Locate and identify every blood parasite.
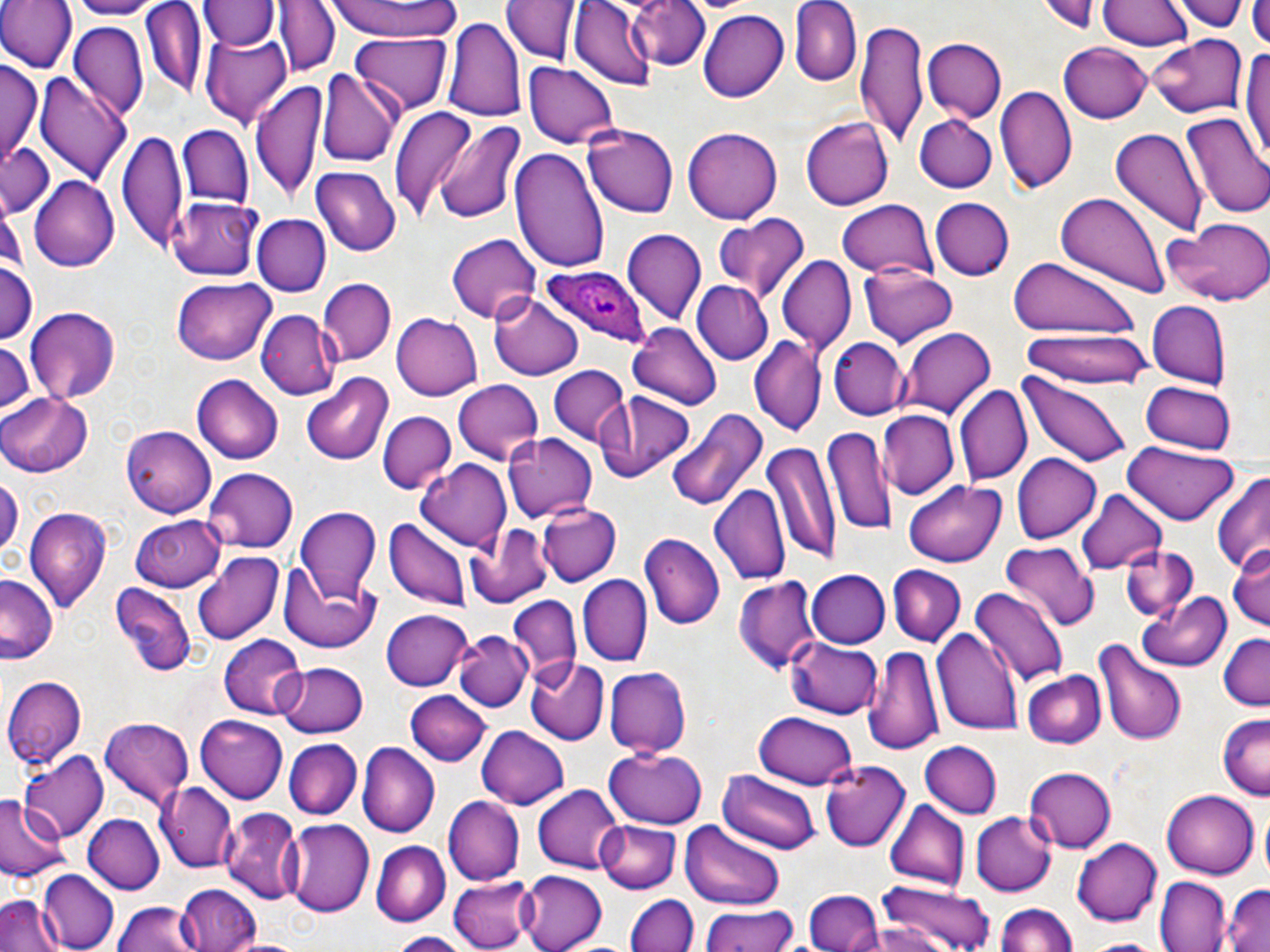
Approximate bounding boxes as (x1,y1)-(x2,y2) corner pairs in pixels.
Plasmodium ovale-infected red blood cells: (543,264)-(653,347).
No Plasmodium falciparum, Plasmodium malariae, Plasmodium vivax, Babesia divergens, or Trypanosoma brucei observed.

Uninfected red blood cell locations: (0,0)-(76,73), (65,0)-(161,18), (202,0)-(274,50), (275,0)-(338,77), (328,0)-(464,42), (787,0)-(860,87), (1039,0)-(1103,34), (1098,0)-(1191,52), (1174,0)-(1249,31), (1249,0)-(1270,48), (503,1)-(578,65), (569,1)-(655,88), (630,1)-(711,72), (139,2)-(207,99), (697,9)-(788,102), (443,17)-(526,125), (856,22)-(926,149), (69,23)-(147,122), (201,26)-(292,125), (353,33)-(451,113), (1146,33)-(1245,117), (920,37)-(1003,121), (1060,42)-(1152,124), (1240,48)-(1269,163), (2,60)-(41,159), (523,62)-(617,149), (319,68)-(400,170), (36,74)-(131,184), (251,78)-(322,209), (998,85)-(1077,194), (389,103)-(475,221), (1180,109)-(1270,221), (915,113)-(999,192), (430,117)-(528,228), (802,117)-(893,210), (177,124)-(253,207), (582,124)-(678,219), (118,127)-(186,252), (682,127)-(783,226), (1110,129)-(1208,235), (2,140)-(56,214), (510,147)-(610,271), (315,165)-(403,256), (29,177)-(119,271), (1054,192)-(1171,298), (166,196)-(263,281), (930,198)-(1014,281), (835,199)-(939,280), (713,213)-(812,302), (251,214)-(330,296), (1165,217)-(1270,306), (622,231)-(706,326), (447,234)-(542,324), (776,254)-(856,352), (1008,255)-(1142,351), (0,256)-(38,345), (859,266)-(958,347), (172,278)-(277,366), (319,280)-(395,364), (694,281)-(772,363), (489,292)-(584,381), (1146,300)-(1231,387), (25,306)-(121,403), (257,309)-(338,399), (391,312)-(483,402), (628,321)-(722,408), (895,326)-(995,422), (1022,331)-(1152,388), (0,336)-(36,420), (748,336)-(825,437), (829,337)-(906,419), (548,366)-(630,448), (302,373)-(394,464), (1014,373)-(1132,470), (194,374)-(282,464), (453,379)-(545,466), (1140,380)-(1237,454), (955,386)-(1031,487), (595,390)-(697,485), (1,392)-(94,478), (666,408)-(770,514), (877,409)-(956,499), (378,410)-(456,494), (822,424)-(896,538), (122,425)-(217,516), (503,432)-(599,524), (765,438)-(839,573), (1122,445)-(1238,527), (1012,452)-(1102,544), (419,457)-(513,553), (201,468)-(297,553), (1210,472)-(1269,580), (0,474)-(22,560), (901,478)-(1008,567), (709,484)-(789,587), (1077,489)-(1167,576), (537,503)-(623,586), (25,506)-(113,613), (296,508)-(383,600), (133,513)-(226,591), (385,519)-(470,609), (465,522)-(552,608), (640,532)-(725,630), (1227,541)-(1270,629), (1000,542)-(1100,631), (1122,545)-(1198,619), (192,552)-(285,645), (278,564)-(379,653), (888,565)-(965,647), (807,569)-(891,648), (0,574)-(62,665), (577,575)-(650,666), (737,577)-(822,676), (110,586)-(195,679), (969,587)-(1070,687), (1139,589)-(1232,671), (507,595)-(579,684), (381,610)-(475,691), (932,624)-(1022,734), (455,630)-(530,713), (1217,632)-(1270,712), (218,636)-(307,720), (786,637)-(881,719), (1091,640)-(1189,746), (864,647)-(944,759), (525,656)-(611,742), (276,661)-(370,738), (603,667)-(690,757), (1023,670)-(1105,748), (3,676)-(88,770), (406,692)-(491,766), (755,710)-(859,790), (1216,714)-(1270,800), (195,716)-(289,802), (99,718)-(194,806), (477,725)-(570,808), (284,739)-(362,819), (919,741)-(1002,819), (359,744)-(438,837), (606,747)-(706,826), (18,750)-(108,842), (819,762)-(910,852), (1024,767)-(1116,854), (719,770)-(821,853), (160,782)-(239,871), (531,784)-(622,873), (1163,788)-(1259,879), (0,793)-(66,885), (443,796)-(524,885), (883,799)-(968,891), (224,807)-(303,907), (968,811)-(1056,897), (82,814)-(164,895), (284,818)-(372,918), (596,820)-(681,892), (682,824)-(785,910), (1073,836)-(1160,927), (372,841)-(449,925), (38,871)-(116,951), (519,871)-(607,952), (447,873)-(535,949), (1156,876)-(1230,952), (875,878)-(996,952), (1222,884)-(1270,952), (175,885)-(261,952), (802,889)-(885,952), (625,893)-(697,952), (0,894)-(63,952), (113,900)-(195,952), (993,904)-(1079,952), (698,907)-(800,952), (384,933)-(469,952), (1079,938)-(1169,952). Slide-level diagnosis: Plasmodium ovale. Single field of view. Thin blood film. May-Grünwald-Giemsa stain. Image is 1270×952 pixels. Light microscopy. 1000x magnification.